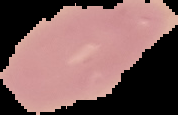
Summary:
  - Malaria status: uninfected
  - Image type: segmented cell region on a black background
  - Preparation: thin blood film
  - Image size: 178×115 pixels